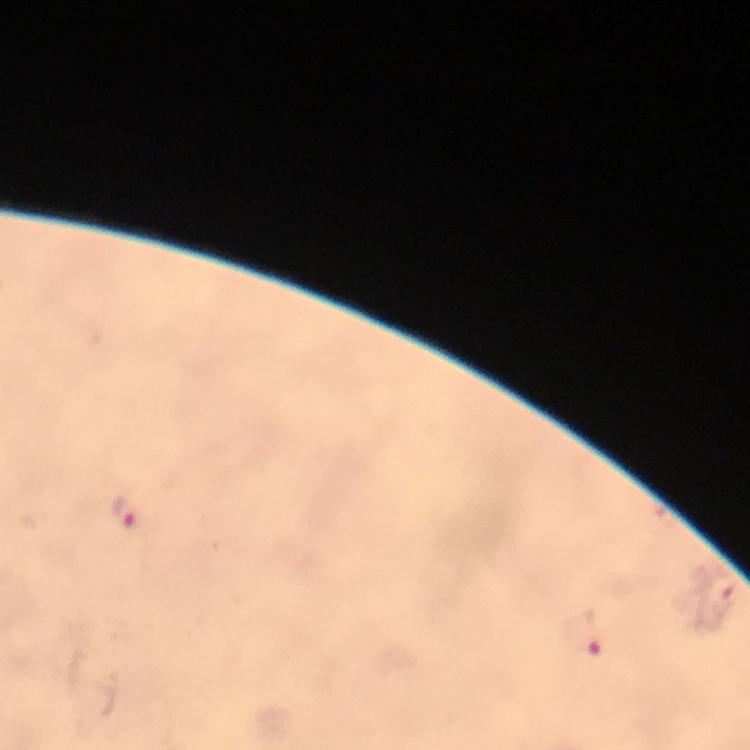

Approximate object centers, in pixels from the top-left corner.
Summary:
  - Plasmodium parasite locations: (x=124, y=512), (x=719, y=593), (x=582, y=633)
  - Stain: Giemsa
  - Immersion oil: used
  - Capture: smartphone mounted on the microscope
  - Preparation: thick blood smear
  - Magnification: 100x
  - Cropped from: one field of view
  - Context: from a diagnostic examination for malaria
  - Image size: 750×750 pixels